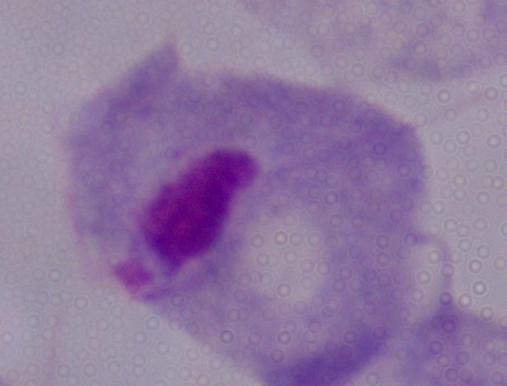
{
  "identification": "trichomonad",
  "modality": "photomicrograph",
  "magnification": "1000x"
}